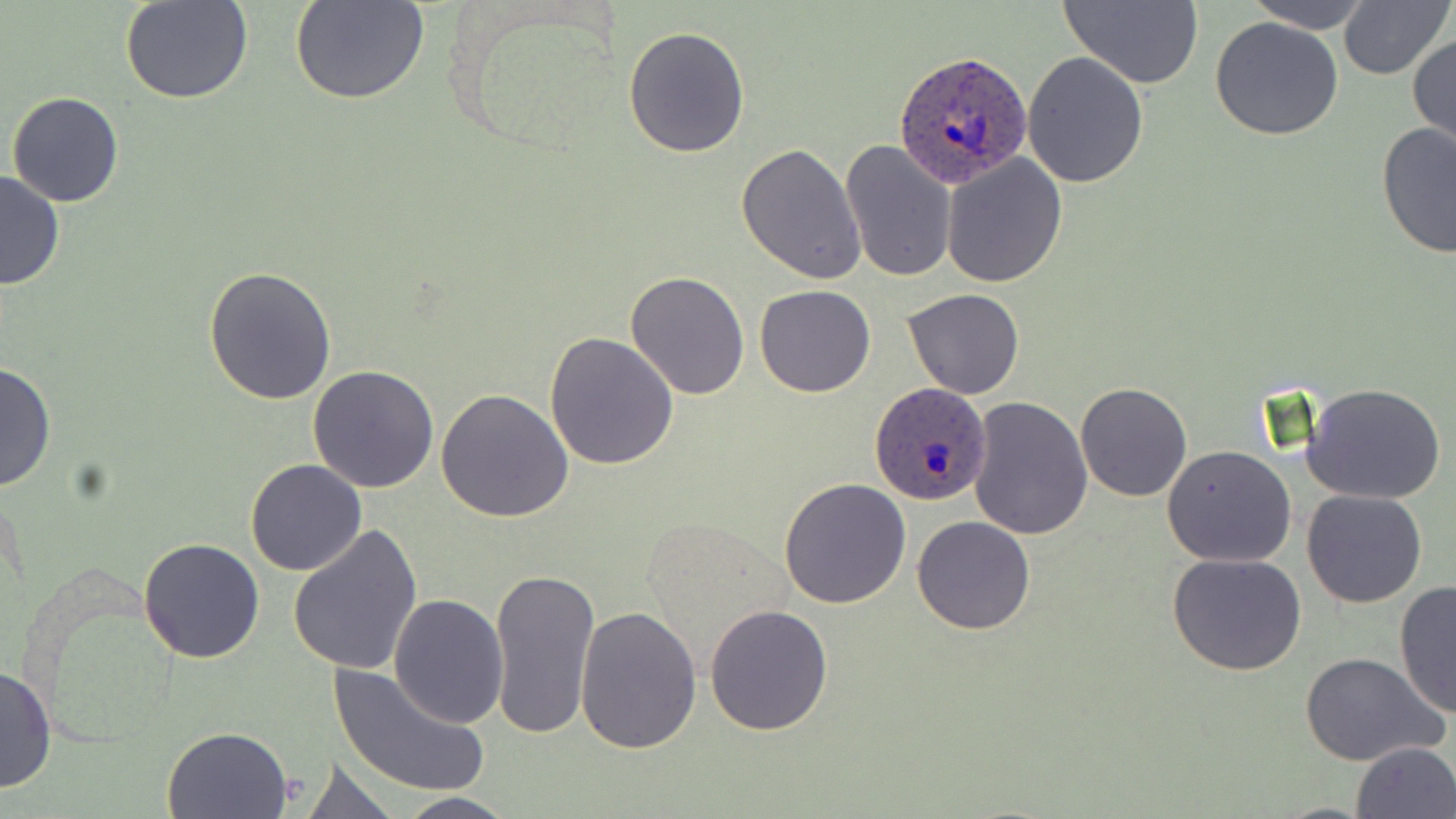

Summary:
  - Coordinate format: approximate bounding boxes as (x1, y1, x2, y2) in pixels
  - Uninfected red blood cell locations: (121, 0, 254, 105), (290, 0, 429, 105), (1058, 0, 1205, 88), (1246, 0, 1369, 32), (1337, 0, 1451, 81), (1209, 16, 1345, 141), (623, 25, 749, 159), (1409, 31, 1456, 157), (1022, 51, 1149, 189), (8, 91, 124, 207), (1376, 121, 1456, 258), (839, 139, 960, 283), (736, 142, 867, 286), (941, 152, 1069, 287), (0, 170, 66, 291), (203, 267, 336, 404), (624, 270, 749, 400), (754, 283, 876, 398), (903, 288, 1026, 399), (544, 331, 680, 469), (0, 360, 56, 492), (308, 366, 439, 494), (1075, 381, 1193, 501), (1300, 381, 1448, 504), (435, 387, 574, 523), (967, 397, 1093, 541), (1162, 445, 1297, 567), (245, 459, 365, 575), (780, 479, 911, 608), (1301, 489, 1428, 608), (913, 515, 1036, 635), (287, 524, 423, 678), (139, 536, 267, 663), (1167, 552, 1309, 677), (486, 567, 601, 744), (1393, 582, 1456, 718), (388, 593, 509, 727), (704, 602, 835, 736), (575, 606, 702, 755), (1302, 653, 1446, 767), (330, 661, 490, 799), (0, 665, 55, 797), (161, 725, 294, 818), (1350, 740, 1456, 819), (295, 755, 401, 818), (385, 791, 521, 819)
  - Plasmodium ovale-infected red blood cell locations: (894, 50, 1032, 187), (869, 382, 992, 506)
  - Slide-level diagnosis: Plasmodium ovale
  - Magnification: 1000x
  - Image size: 1456×819 pixels
  - Modality: optical microscopy
  - Preparation: thin blood film
  - Stain: May-Grünwald-Giemsa
  - Field of view: one of a larger specimen